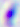
Summary:
  - Modality: micrograph
  - Identification: Toxoplasma gondii
  - Magnification: 400x